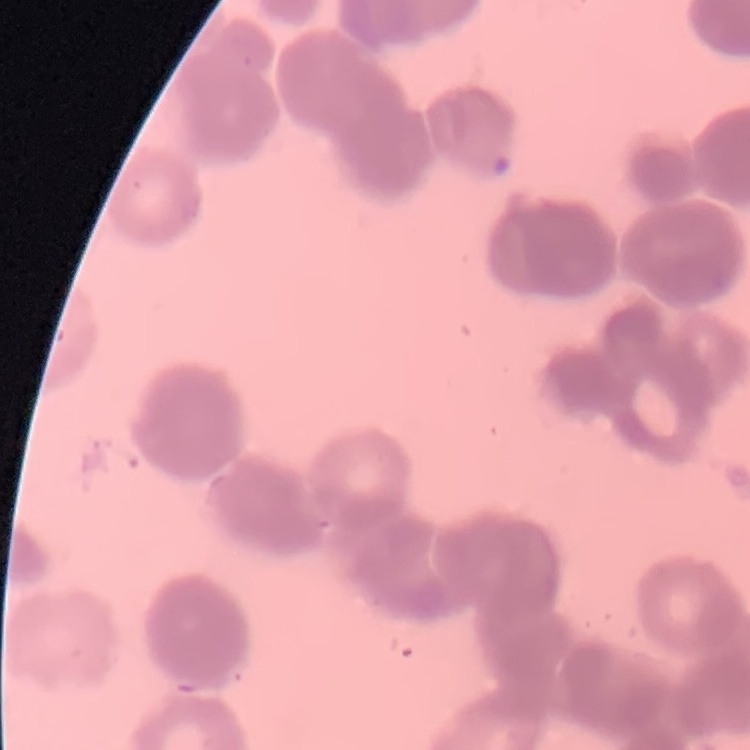
The red blood cells show rouleaux formation. Thin blood film. Square crop of a larger photomicrograph. Field's or Giemsa stain.